Locate every malaria parasite and every leukocyte.
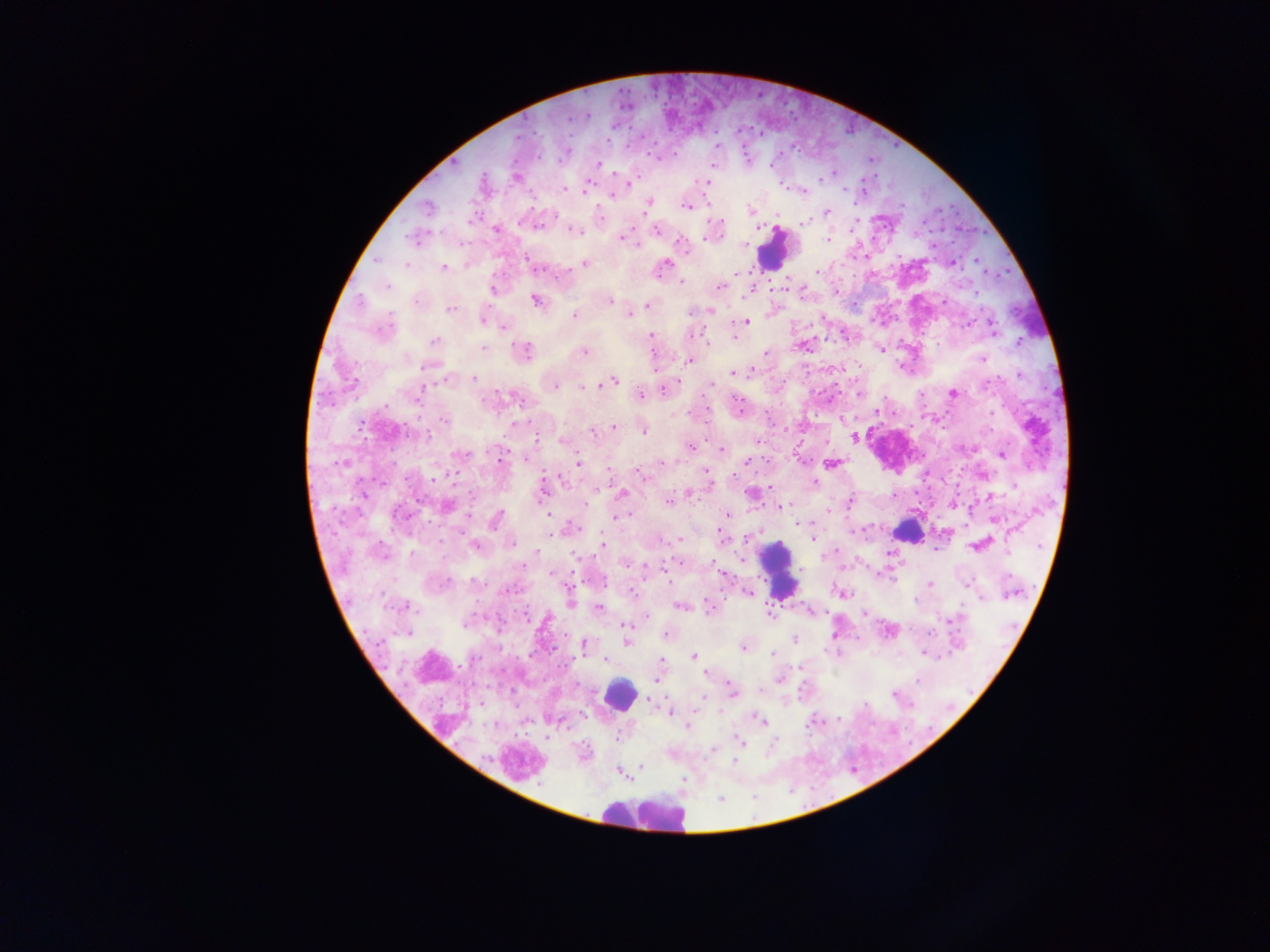

Approximate centers as {x, y} in pixels.
Malaria parasites: {586, 115}, {715, 146}, {746, 160}, {712, 162}, {598, 163}, {772, 164}, {832, 172}, {516, 177}, {629, 182}, {707, 182}, {587, 184}, {564, 188}, {584, 191}, {802, 191}, {613, 194}, {646, 205}, {685, 205}, {428, 208}, {750, 210}, {826, 213}, {805, 222}, {496, 228}, {574, 229}, {656, 230}, {623, 237}, {827, 239}, {682, 244}, {977, 260}, {951, 263}, {584, 264}, {406, 266}, {535, 266}, {443, 267}, {661, 269}, {816, 272}, {680, 281}, {719, 286}, {492, 287}, {784, 288}, {750, 289}, {835, 289}, {416, 300}, {535, 300}, {609, 300}, {647, 305}, {449, 309}, {710, 311}, {629, 313}, {575, 315}, {483, 318}, {745, 321}, {990, 322}, {505, 327}, {382, 328}, {992, 330}, {691, 332}, {734, 335}, {650, 337}, {434, 342}, {803, 345}, {482, 347}, {881, 348}, {584, 351}, {522, 352}, {766, 353}, {983, 359}, {690, 360}, {426, 365}, {734, 373}, {1019, 374}, {445, 377}, {473, 378}, {612, 381}, {554, 385}, {710, 385}, {583, 387}, {664, 388}, {418, 393}, {859, 393}, {953, 393}, {640, 395}, {876, 411}, {444, 420}, {841, 420}, {614, 426}, {642, 429}, {593, 431}, {853, 438}, {561, 440}, {756, 442}, {690, 447}, {721, 449}, {1002, 454}, {460, 455}, {526, 457}, {500, 460}, {799, 460}, {746, 461}, {662, 462}, {578, 463}, {831, 463}, {706, 473}, {640, 474}, {981, 474}, {813, 483}, {770, 487}, {541, 488}, {621, 493}, {688, 493}, {750, 493}, {893, 495}, {849, 501}, {668, 502}, {952, 503}, {781, 505}, {447, 506}, {827, 511}, {548, 512}, {726, 514}, {615, 517}, {994, 519}, {495, 521}, {572, 528}, {551, 534}, {680, 539}, {721, 539}, {813, 539}, {511, 542}, {474, 545}, {603, 545}, {979, 545}, {936, 548}, {537, 553}, {626, 562}, {679, 563}, {647, 566}, {721, 573}, {552, 574}, {966, 583}, {929, 584}, {631, 592}, {748, 592}, {842, 593}, {570, 602}, {400, 606}, {708, 606}, {681, 607}, {599, 608}, {810, 612}, {769, 613}, {863, 614}, {646, 615}, {950, 620}, {466, 622}, {623, 624}, {888, 630}, {407, 631}, {835, 633}, {927, 633}, {665, 634}, {794, 638}, {626, 641}, {584, 646}, {743, 647}, {924, 653}, {773, 654}, {693, 656}, {606, 660}, {706, 672}, {779, 678}, {656, 679}, {732, 692}, {894, 694}, {648, 699}, {480, 703}, {669, 711}, {757, 719}, {761, 721}, {686, 726}, {739, 741}, {711, 748}, {640, 765}, {619, 772}.
Leukocytes: {772, 249}, {907, 531}, {779, 568}, {618, 693}, {643, 814}.

Summary:
  - Image size: 1270×952 pixels
  - Preparation: thick blood film
  - Country: Ghana
  - Field of view: single
  - Capture: mobile-phone photograph through a microscope